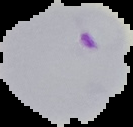
Summary:
  - Image type: segmented cell region on a black background
  - Preparation: thin blood film
  - Malaria status: parasitized
  - Image size: 133×127 pixels